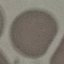 Malaria status: uninfected. Automatically extracted cell patch, resized to 64 × 64 pixels. Giemsa stain. Acquired by smartphone through the microscope eyepiece. Thin blood smear.